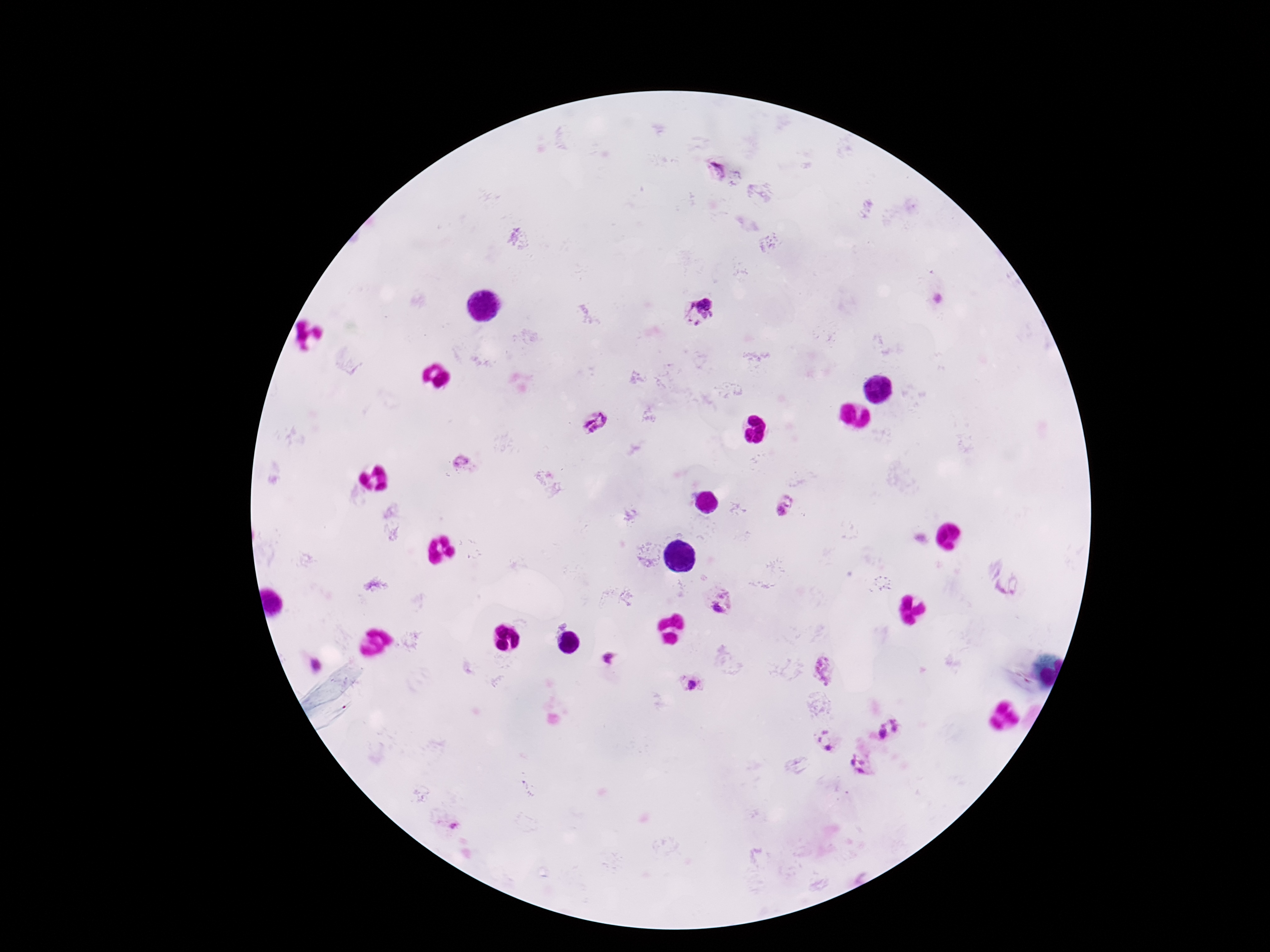
Approximate centers as [x, y] in pixels.
Summary:
  - Plasmodium parasite locations: [716, 171], [701, 312], [598, 421], [461, 460], [784, 506], [724, 602], [609, 659], [825, 671], [692, 685], [899, 723], [880, 732], [823, 736], [829, 748], [859, 762]
  - Magnification: 100x
  - Preparation: thick blood smear
  - Image size: 1270×952 pixels
  - Field of view: one from this slide
  - Patient malaria status: positive
  - Stain: Giemsa
  - Capture: smartphone camera through the microscope eyepiece